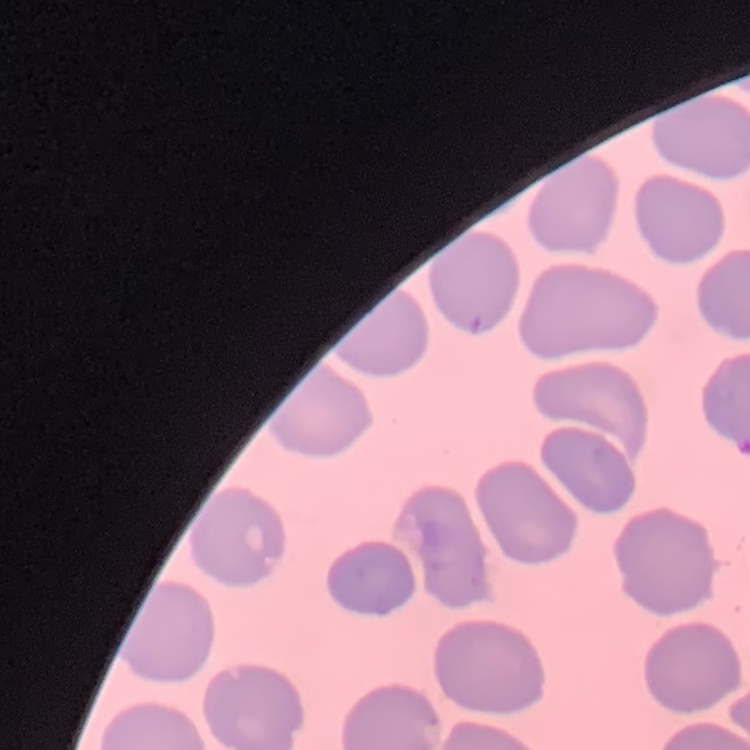 The erythrocytes exhibit no rouleaux formation. One tile cut from a larger photomicrograph. Thin blood smear. Field's or Giemsa stain.